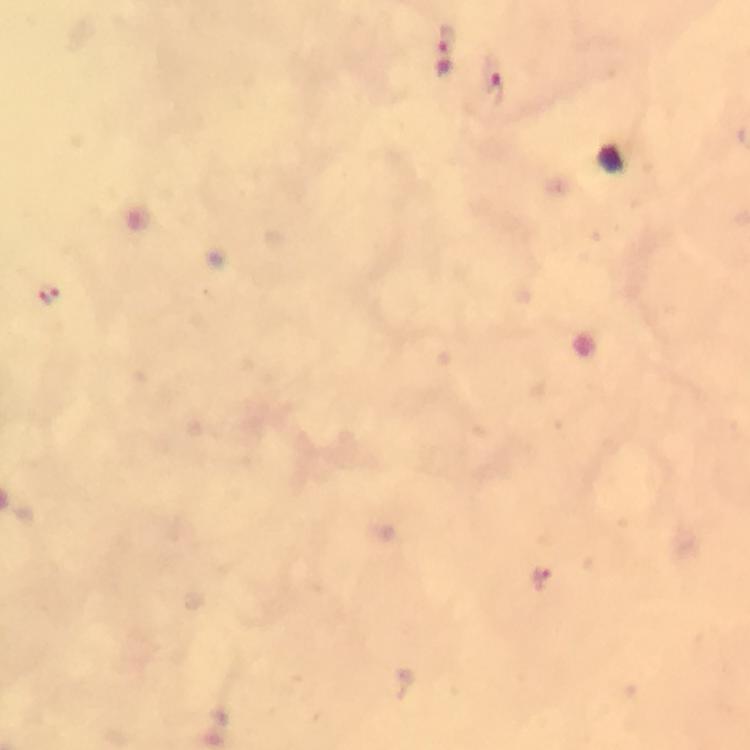
Approximate object centers, in pixels from the top-left corner.
Summary:
  - Plasmodium parasite locations: (x=442, y=51), (x=491, y=88), (x=47, y=294), (x=540, y=579)
  - Stain: Giemsa
  - Magnification: 100x
  - Capture: smartphone photograph through a microscope
  - Preparation: thick smear
  - Immersion oil: used
  - Context: from a malaria diagnostic workup
  - Image size: 750×750 pixels
  - Cropped from: one field of view